Locate every Plasmodium parasite.
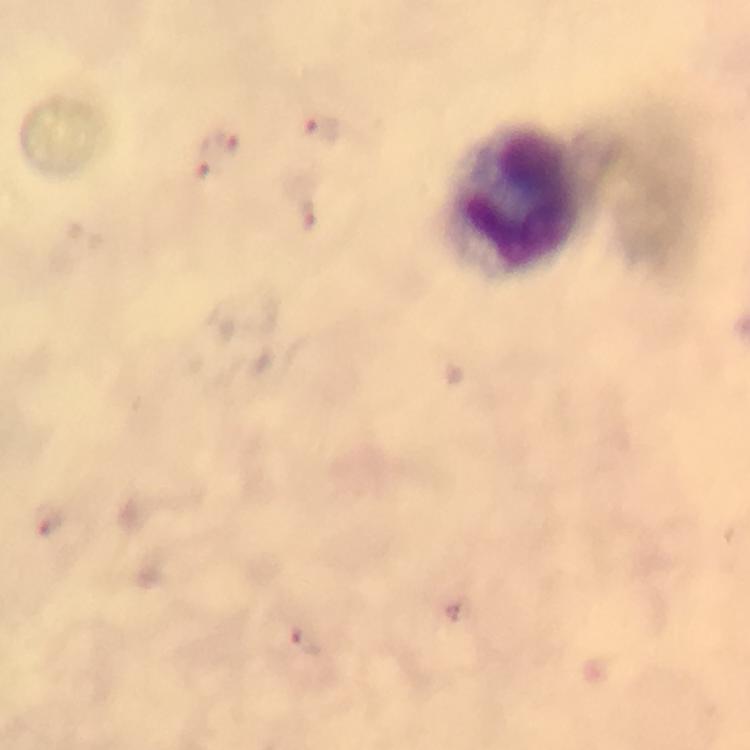
Approximate object centers, in pixels from the top-left corner.
Plasmodium parasites: (x=324, y=127), (x=224, y=139), (x=309, y=216), (x=307, y=641).

Leukocyte locations: (x=512, y=196). From a diagnostic examination for malaria. Photographed with a smartphone mounted on the microscope. A crop from one field of view. At 100x magnification. Immersion oil applied. Giemsa stain. Thick smear. Image is 750×750 pixels.